Outline each blood parasite and name the species.
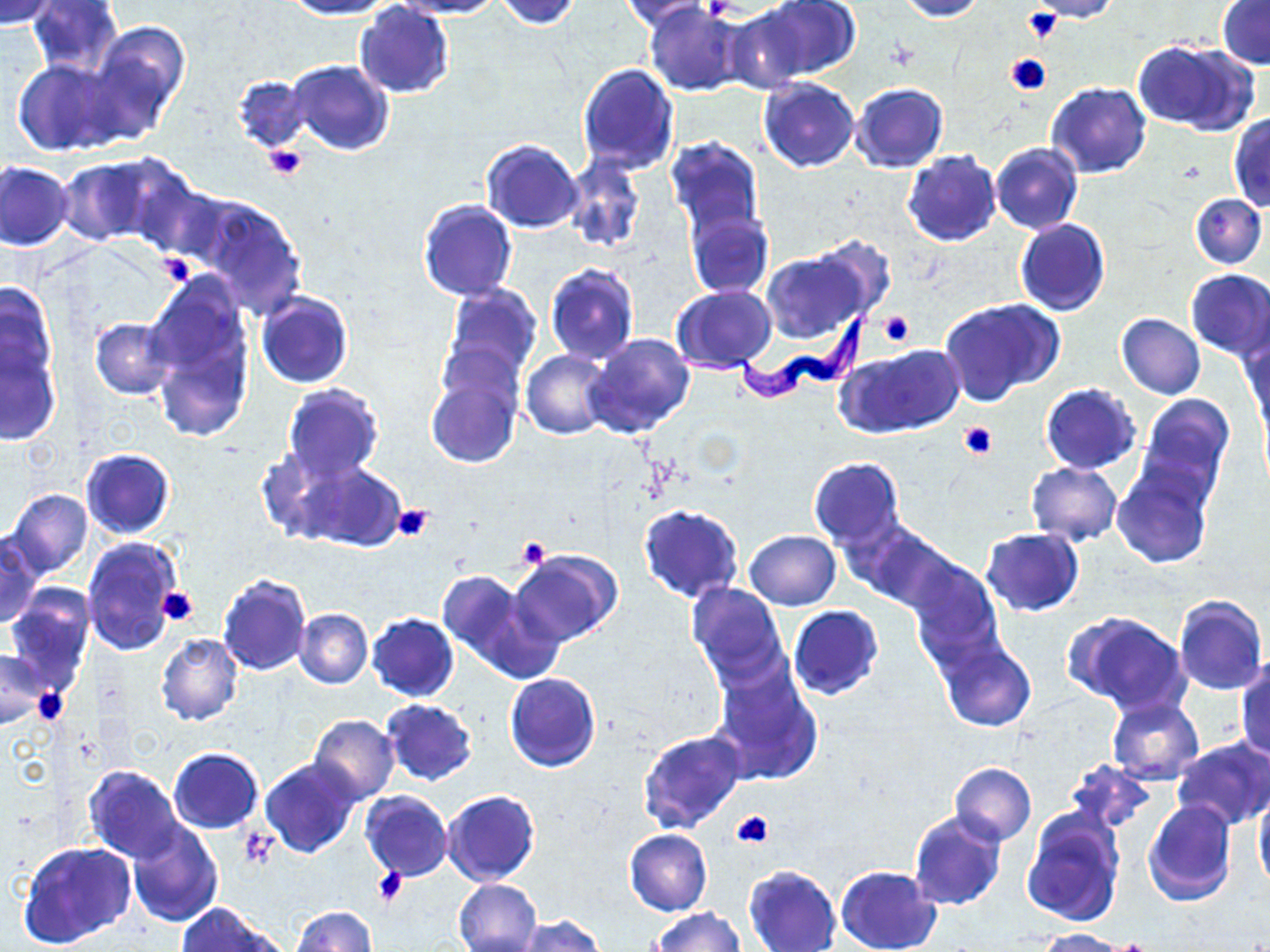

Approximate bounding boxes as [x1, y1, x2, y2] in pixels.
Trypanosoma brucei: [674, 307, 869, 410].
No Plasmodium falciparum, Plasmodium ovale, Plasmodium malariae, Plasmodium vivax, or Babesia divergens observed.

Summary:
  - Platelet locations: [1023, 9, 1061, 44], [1004, 52, 1052, 94], [263, 145, 306, 180], [157, 254, 195, 287], [878, 310, 916, 347], [959, 421, 998, 458], [390, 501, 436, 542], [517, 536, 550, 570], [157, 587, 200, 626], [33, 687, 67, 725], [732, 809, 774, 849], [238, 828, 277, 871], [373, 867, 406, 906]
  - Uninfected red blood cell locations: [0, 0, 63, 26], [26, 0, 124, 79], [284, 0, 395, 19], [397, 0, 505, 18], [494, 0, 582, 28], [621, 0, 716, 32], [761, 0, 858, 79], [896, 0, 986, 21], [1025, 0, 1122, 22], [1218, 2, 1270, 70], [354, 3, 455, 100], [645, 4, 744, 97], [726, 9, 813, 91], [88, 23, 190, 136], [1134, 39, 1255, 133], [12, 56, 123, 156], [289, 60, 394, 155], [578, 63, 679, 176], [232, 73, 310, 154], [758, 77, 860, 172], [850, 82, 949, 173], [1047, 82, 1151, 178], [1228, 113, 1270, 212], [665, 137, 765, 239], [481, 140, 583, 233], [1002, 141, 1094, 315], [991, 142, 1082, 235], [902, 150, 999, 246], [565, 153, 645, 255], [59, 156, 169, 245], [0, 161, 75, 251], [123, 168, 227, 263], [191, 193, 308, 318], [1189, 193, 1266, 270], [419, 200, 518, 301], [685, 206, 774, 300], [1015, 218, 1110, 317], [807, 232, 899, 322], [761, 252, 866, 343], [545, 264, 638, 364], [1185, 269, 1270, 360], [146, 272, 257, 433], [0, 280, 59, 391], [443, 284, 542, 381], [672, 285, 777, 372], [255, 291, 353, 389], [939, 296, 1063, 405], [436, 312, 537, 440], [1116, 313, 1205, 398], [91, 318, 178, 399], [1242, 330, 1270, 433], [585, 334, 696, 439], [1, 341, 62, 446], [843, 344, 963, 438], [522, 350, 614, 439], [425, 352, 522, 471], [1041, 383, 1140, 473], [281, 384, 385, 483], [1136, 393, 1233, 501], [80, 448, 175, 539], [808, 457, 905, 550], [291, 460, 405, 552], [1025, 462, 1122, 547], [1112, 465, 1213, 569], [5, 488, 94, 581], [639, 504, 743, 603], [849, 522, 964, 616], [981, 527, 1084, 615], [744, 529, 840, 610], [0, 533, 43, 628], [83, 536, 184, 656], [508, 550, 620, 647], [907, 559, 1004, 668], [437, 570, 544, 679], [217, 574, 312, 675], [686, 583, 787, 685], [5, 587, 95, 691], [1172, 593, 1267, 696], [788, 606, 883, 700], [294, 608, 373, 688], [367, 613, 459, 702], [1064, 613, 1192, 716], [156, 634, 243, 726], [937, 639, 1036, 732], [0, 647, 48, 728], [1235, 658, 1270, 760], [710, 660, 824, 786], [505, 673, 600, 773], [1106, 695, 1203, 784], [381, 699, 478, 786], [307, 715, 401, 802], [637, 730, 747, 834], [1171, 738, 1270, 830], [168, 748, 263, 832], [261, 757, 361, 858], [1067, 758, 1155, 834], [949, 763, 1037, 845], [83, 764, 183, 861], [1254, 789, 1270, 891], [360, 790, 453, 881], [440, 790, 540, 886], [1142, 799, 1237, 906], [1021, 808, 1126, 928], [909, 811, 1007, 912], [127, 821, 223, 927], [624, 829, 712, 914], [19, 841, 135, 950], [743, 865, 841, 951], [835, 866, 941, 952], [453, 878, 542, 952], [175, 904, 279, 951], [291, 906, 377, 951], [652, 907, 745, 952], [515, 917, 606, 952], [1037, 928, 1128, 952]
  - Slide-level diagnosis: Trypanosoma brucei
  - Modality: optical microscopy
  - Preparation: thin blood film
  - Field of view: one of a larger specimen
  - Magnification: 1000x
  - Stain: May-Grünwald-Giemsa
  - Image size: 1270×952 pixels